Assess this cell for malaria.
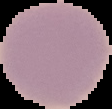

Uninfected.

preparation = thin blood smear
image type = cell region segmented out of the field of view; surrounding area masked to black
image size = 112×109 pixels